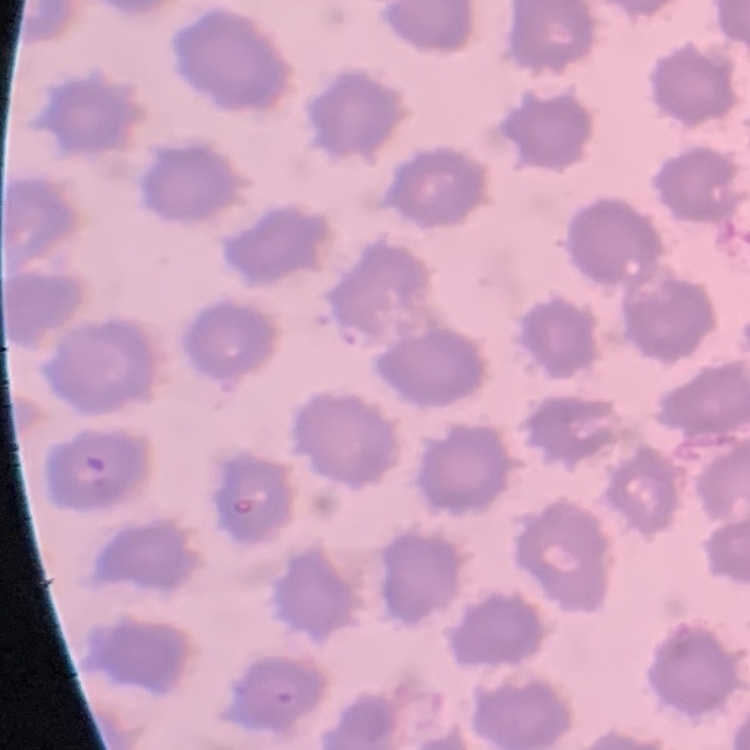
{
  "erythrocyte_morphology": "no rouleaux formation",
  "preparation": "thin blood smear",
  "stain": "Field's or Giemsa",
  "image_type": "square crop of a larger photomicrograph"
}